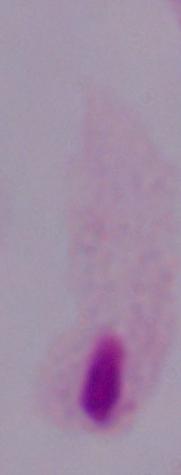
A trichomonad is shown. Micrograph. 1000x magnification.